Report the malaria status of this cell.
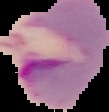

Parasitized.

Image is 109×112 pixels. From a thin blood smear. The area outside the segmented cell region is set to black.